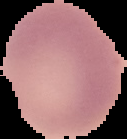
From a thin blood smear. Image is 127×139 pixels. Malaria status: uninfected. Cell region segmented out of the field of view; the surrounding area is masked to black.